Find the cells and give the type of each one.
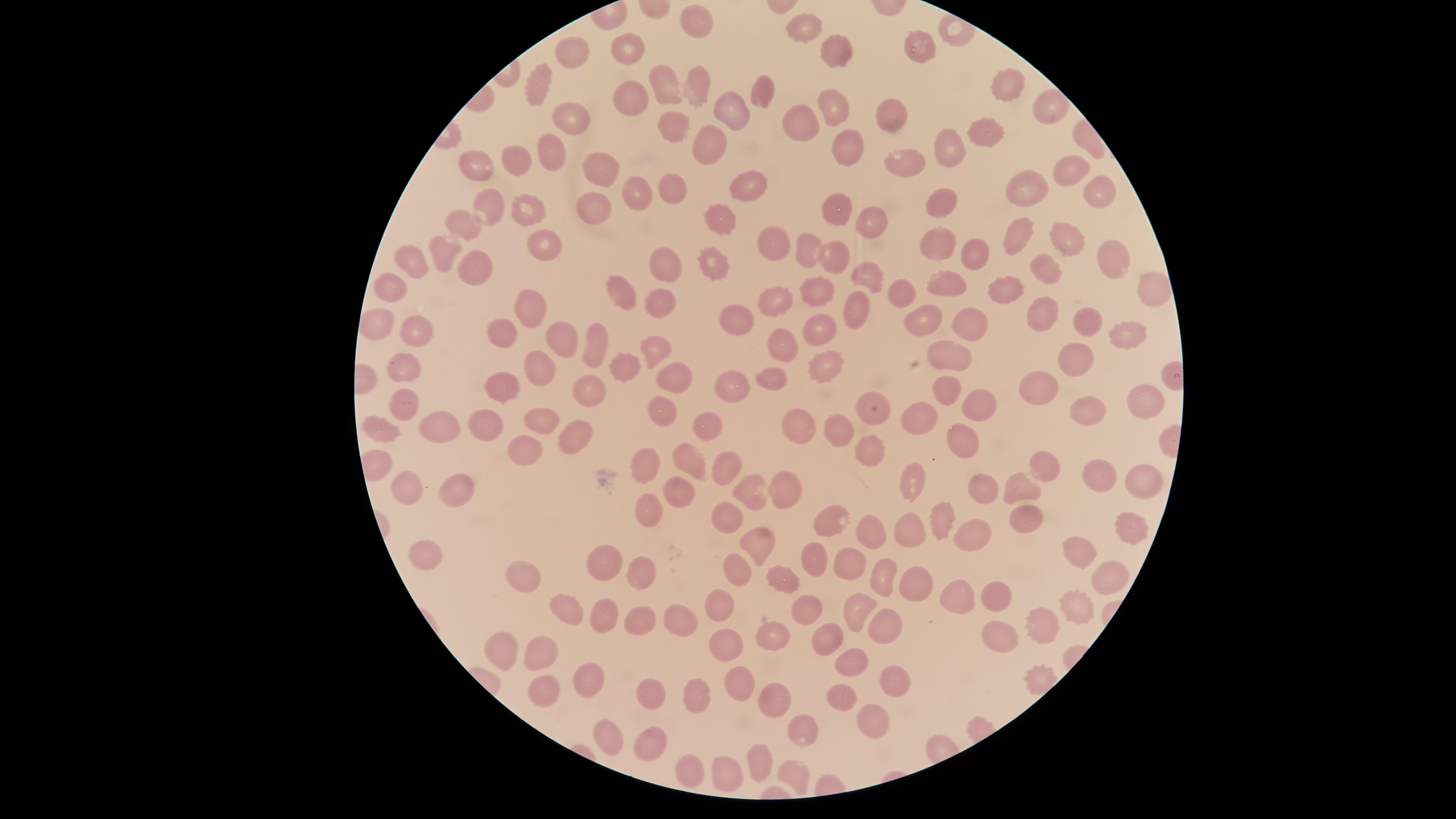

No parasitized red blood cells identified.
Approximate marker points, in pixels from the top-left corner.
Uninfected red blood cells: (x=697, y=20), (x=809, y=29), (x=922, y=44), (x=632, y=50), (x=576, y=51), (x=828, y=51), (x=662, y=80), (x=1000, y=85), (x=693, y=87), (x=535, y=89), (x=760, y=93), (x=627, y=99), (x=834, y=102), (x=729, y=107), (x=1047, y=108), (x=566, y=110), (x=889, y=117), (x=799, y=120), (x=675, y=121), (x=988, y=138), (x=707, y=141), (x=848, y=144), (x=541, y=148), (x=947, y=152), (x=518, y=156), (x=476, y=163), (x=599, y=167), (x=908, y=167), (x=1057, y=169), (x=742, y=181), (x=1025, y=185), (x=1094, y=186), (x=668, y=188), (x=634, y=190), (x=942, y=202), (x=528, y=206), (x=593, y=207), (x=837, y=207), (x=483, y=211), (x=718, y=217), (x=464, y=221), (x=870, y=221), (x=1017, y=230), (x=1066, y=238), (x=932, y=239), (x=769, y=243), (x=544, y=244), (x=806, y=250), (x=972, y=250), (x=442, y=252), (x=1108, y=253), (x=831, y=254), (x=719, y=258), (x=662, y=261), (x=408, y=262), (x=474, y=266), (x=1040, y=270), (x=863, y=273), (x=947, y=283), (x=392, y=284), (x=1011, y=287), (x=820, y=289), (x=905, y=289), (x=620, y=291), (x=1145, y=291), (x=783, y=295), (x=661, y=303), (x=538, y=307), (x=855, y=308), (x=1042, y=312), (x=732, y=318), (x=934, y=318), (x=1085, y=320), (x=379, y=321), (x=974, y=324), (x=817, y=328), (x=1120, y=328), (x=414, y=329), (x=502, y=330), (x=559, y=339), (x=593, y=342), (x=786, y=346), (x=653, y=348), (x=950, y=355), (x=1070, y=356), (x=823, y=359), (x=405, y=365), (x=538, y=369), (x=623, y=371), (x=672, y=376), (x=775, y=381), (x=1037, y=381), (x=507, y=383), (x=734, y=383), (x=946, y=386), (x=588, y=391), (x=1140, y=397), (x=402, y=401), (x=987, y=406), (x=1078, y=410), (x=662, y=411), (x=874, y=414), (x=535, y=417), (x=923, y=418), (x=708, y=423), (x=795, y=426), (x=480, y=427), (x=442, y=428), (x=841, y=428), (x=386, y=432), (x=581, y=433), (x=961, y=436), (x=525, y=452), (x=871, y=452), (x=690, y=460), (x=643, y=464), (x=1044, y=465), (x=726, y=467), (x=1089, y=476), (x=916, y=480), (x=405, y=483), (x=1136, y=483), (x=456, y=488), (x=746, y=488), (x=983, y=488), (x=1020, y=488), (x=784, y=491), (x=680, y=494), (x=644, y=504), (x=723, y=510), (x=1023, y=516), (x=937, y=517), (x=829, y=518), (x=1126, y=525), (x=866, y=531), (x=911, y=532), (x=970, y=535), (x=754, y=541), (x=1076, y=551), (x=816, y=555), (x=430, y=556), (x=603, y=562), (x=847, y=562), (x=645, y=571), (x=734, y=573), (x=1106, y=573), (x=531, y=577), (x=881, y=579), (x=779, y=582), (x=917, y=584), (x=994, y=592), (x=957, y=598), (x=563, y=603), (x=720, y=603), (x=1069, y=606), (x=861, y=607), (x=805, y=608), (x=602, y=612), (x=675, y=616), (x=638, y=617), (x=882, y=627), (x=1040, y=631), (x=777, y=632), (x=994, y=632), (x=828, y=639), (x=546, y=647), (x=729, y=651), (x=509, y=655), (x=853, y=659), (x=892, y=678), (x=587, y=680), (x=736, y=683), (x=540, y=689), (x=656, y=694), (x=701, y=695), (x=774, y=696), (x=843, y=698), (x=867, y=718), (x=798, y=727), (x=604, y=731), (x=650, y=741), (x=763, y=761), (x=686, y=766), (x=730, y=777), (x=799, y=777).
No white blood cells identified.

field of view = single
capture = smartphone photograph through the microscope eyepiece
stain = Giemsa
image size = 1456×819 pixels
preparation = thin smear of blood
visible region = circular